Name the cell type shown.
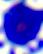

This is a leukocyte.

{
  "modality": "photomicrograph",
  "magnification": "400x"
}